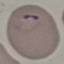

Malaria status: parasitized. Photographed with a smartphone camera at the microscope eyepiece. Giemsa stain. Automatically extracted cell patch, resized to 64 × 64 pixels. Thin smear of blood.